Identify the preparation type.
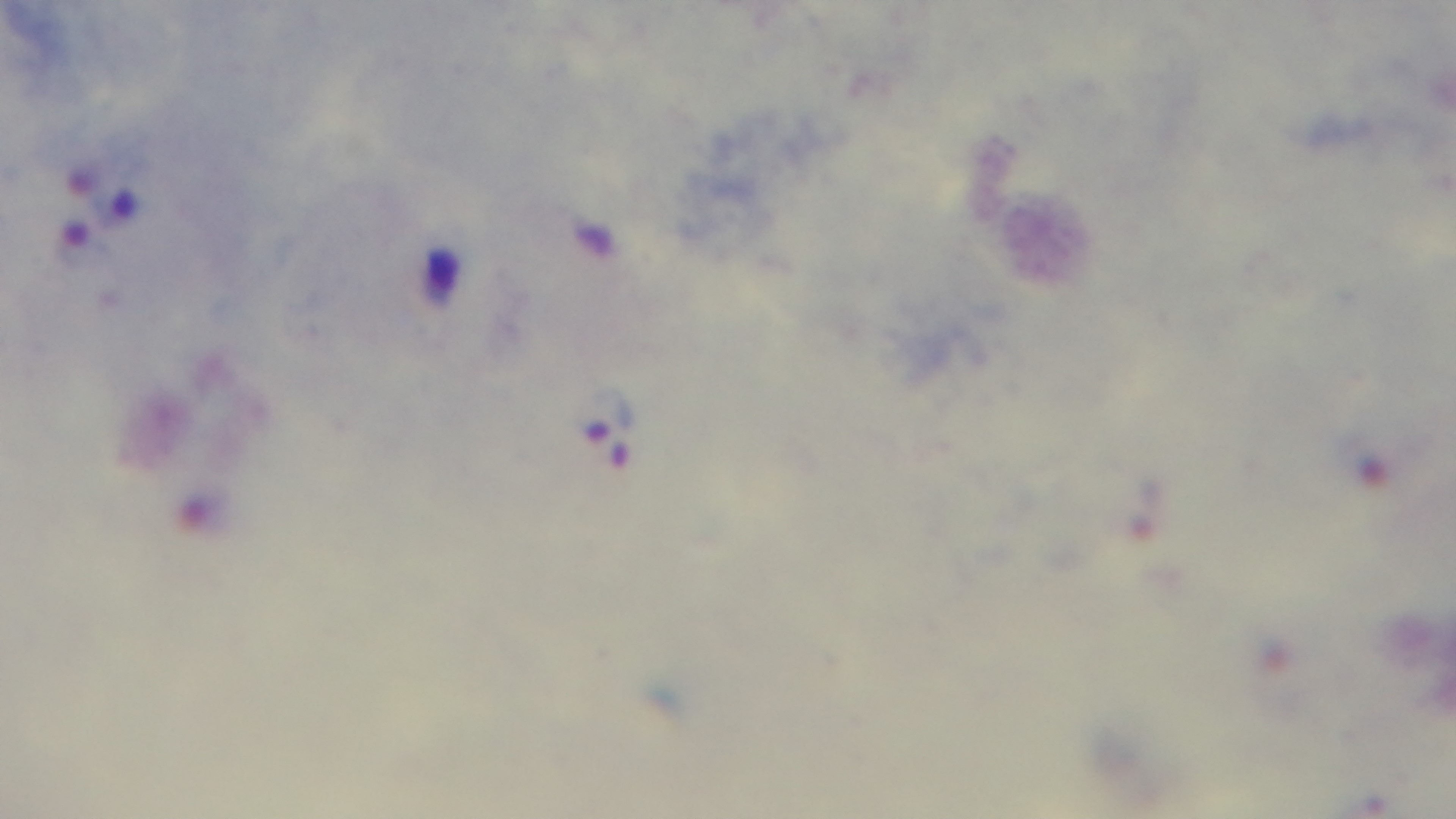
It is a thick blood film.

Malaria status: positive. One field from the slide. 100x oil-immersion objective. Giemsa stain. Mounted 4K digital camera. Photomicrograph.